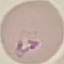
Result: malaria parasites detected. Giemsa-stained preparation. Acquired by smartphone through the microscope eyepiece. Thin smear of blood. Automatically extracted cell patch, resized to 64 × 64 pixels.